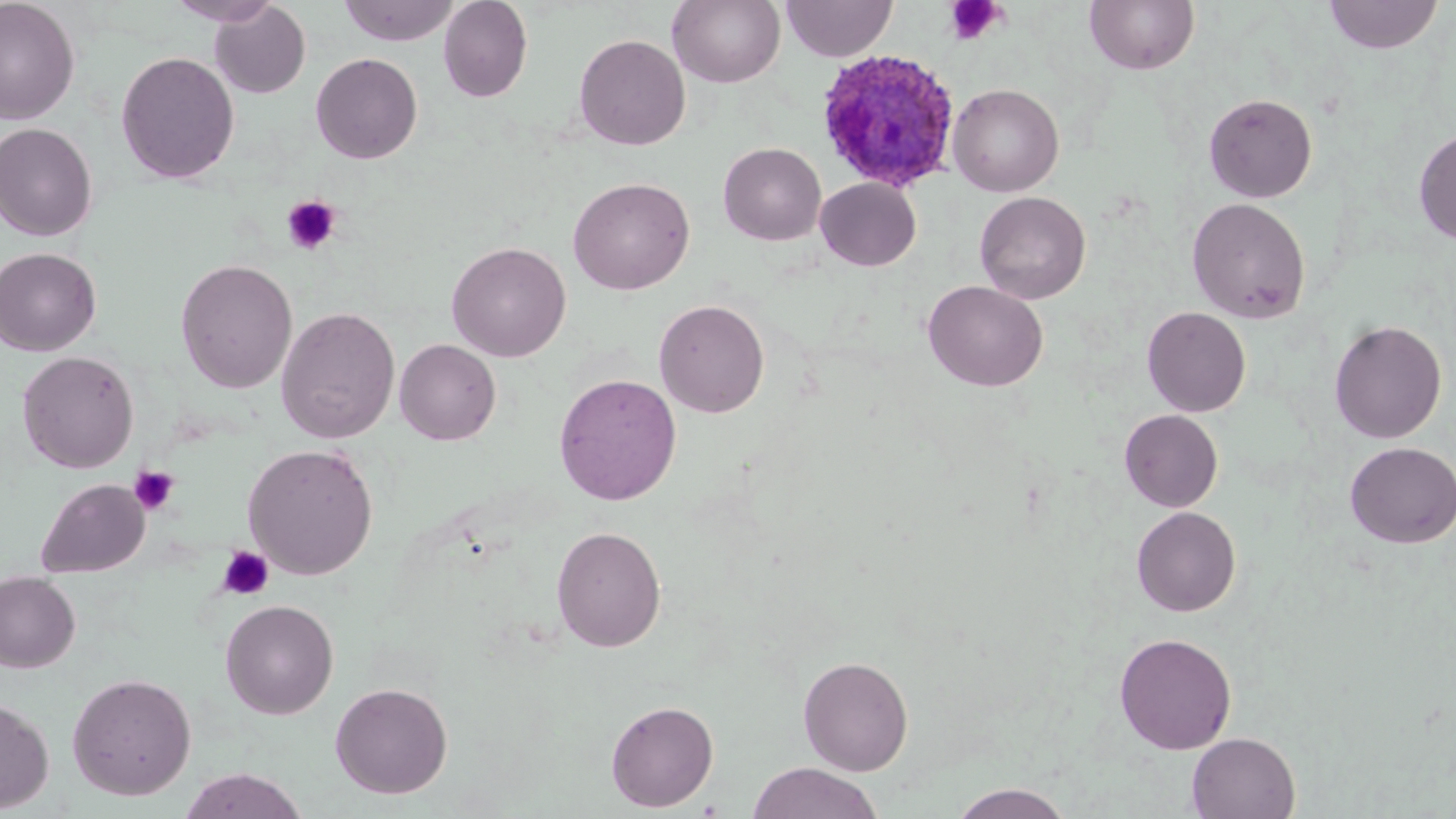

Approximate bounding boxes as (x1, y1, x2, y2) in pixels. Platelet locations: (944, 0, 1005, 45), (281, 195, 342, 255), (129, 465, 180, 516), (217, 545, 275, 600). Plasmodium ovale-infected red blood cell locations: (816, 49, 961, 192). Uninfected red blood cell locations: (165, 0, 283, 26), (338, 0, 460, 46), (438, 0, 533, 103), (668, 0, 785, 88), (781, 0, 897, 62), (1084, 0, 1200, 75), (1323, 0, 1444, 54), (0, 1, 80, 125), (209, 2, 311, 99), (573, 33, 691, 150), (116, 51, 239, 185), (310, 52, 423, 164), (948, 83, 1064, 197), (1203, 92, 1318, 203), (0, 122, 98, 242), (1413, 127, 1456, 245), (718, 142, 826, 246), (568, 176, 695, 295), (816, 177, 921, 271), (974, 191, 1092, 305), (1187, 197, 1311, 324), (447, 241, 572, 362), (0, 247, 102, 356), (175, 258, 298, 394), (923, 280, 1048, 392), (654, 298, 770, 418), (276, 306, 400, 444), (1142, 306, 1251, 417), (1329, 319, 1447, 443), (394, 339, 501, 445), (17, 351, 139, 473), (553, 372, 682, 505), (1119, 409, 1223, 512), (1344, 441, 1456, 548), (242, 443, 380, 580), (35, 478, 150, 577), (1131, 505, 1241, 616), (551, 525, 667, 653), (0, 571, 81, 673), (220, 599, 339, 719), (1113, 632, 1238, 753), (798, 655, 914, 775), (66, 672, 197, 800), (330, 682, 453, 798), (0, 696, 55, 813), (605, 699, 719, 811), (1186, 732, 1301, 818), (747, 762, 883, 819), (178, 768, 309, 819), (948, 784, 1076, 819). Slide-level diagnosis: Plasmodium ovale. Thin blood film. Optical microscopy. Image is 1456×819 pixels. One field of a larger specimen. May-Grünwald-Giemsa stain. 1000x magnification.